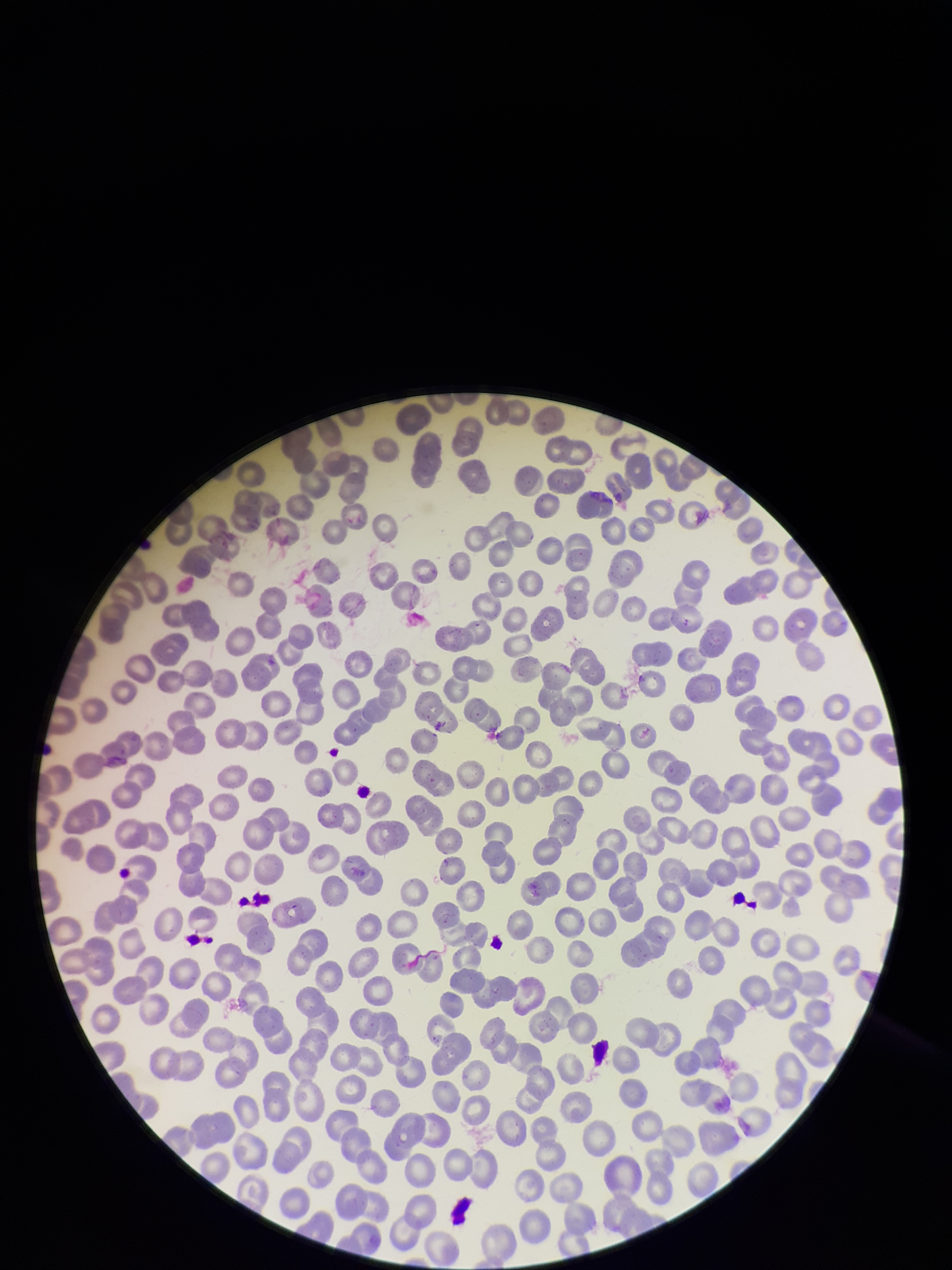

Parasitized red blood cells: none seen. Preparation: thin smear. Image is 952×1270 pixels. Smartphone photograph taken through the eyepiece of a microscope. Giemsa stain. Patient malaria status: negative. One field from this slide. Parasitized red blood cell count: 0. Red blood cell count: 319.